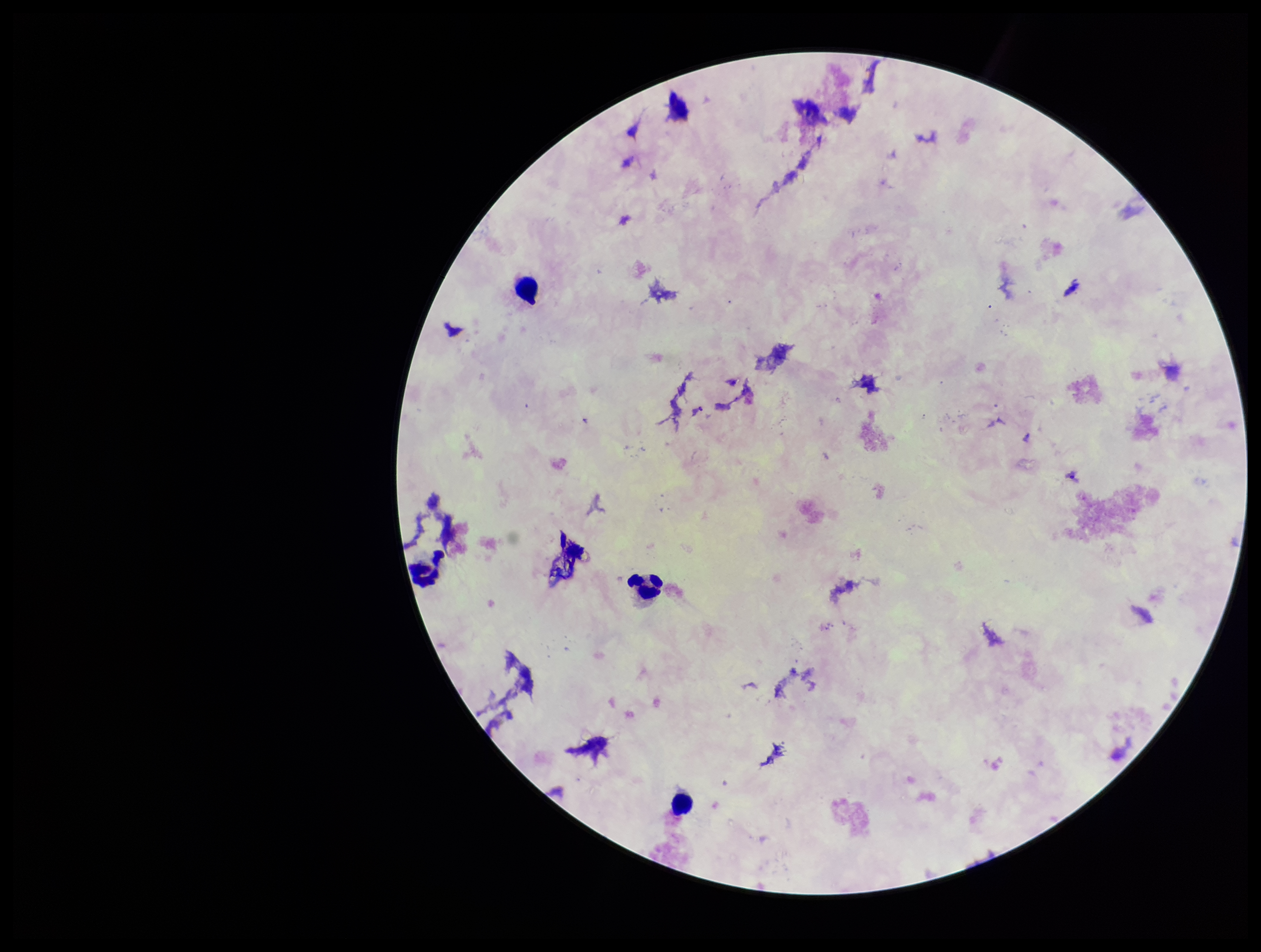 Preparation: thick smear. Smartphone photograph taken through the eyepiece of a microscope. Leukocyte count: 4. One field from this slide. Image is 1261×952 pixels. Parasite count: 0. Stained with Giemsa. Plasmodium parasites: none identified. Patient malaria status: negative.